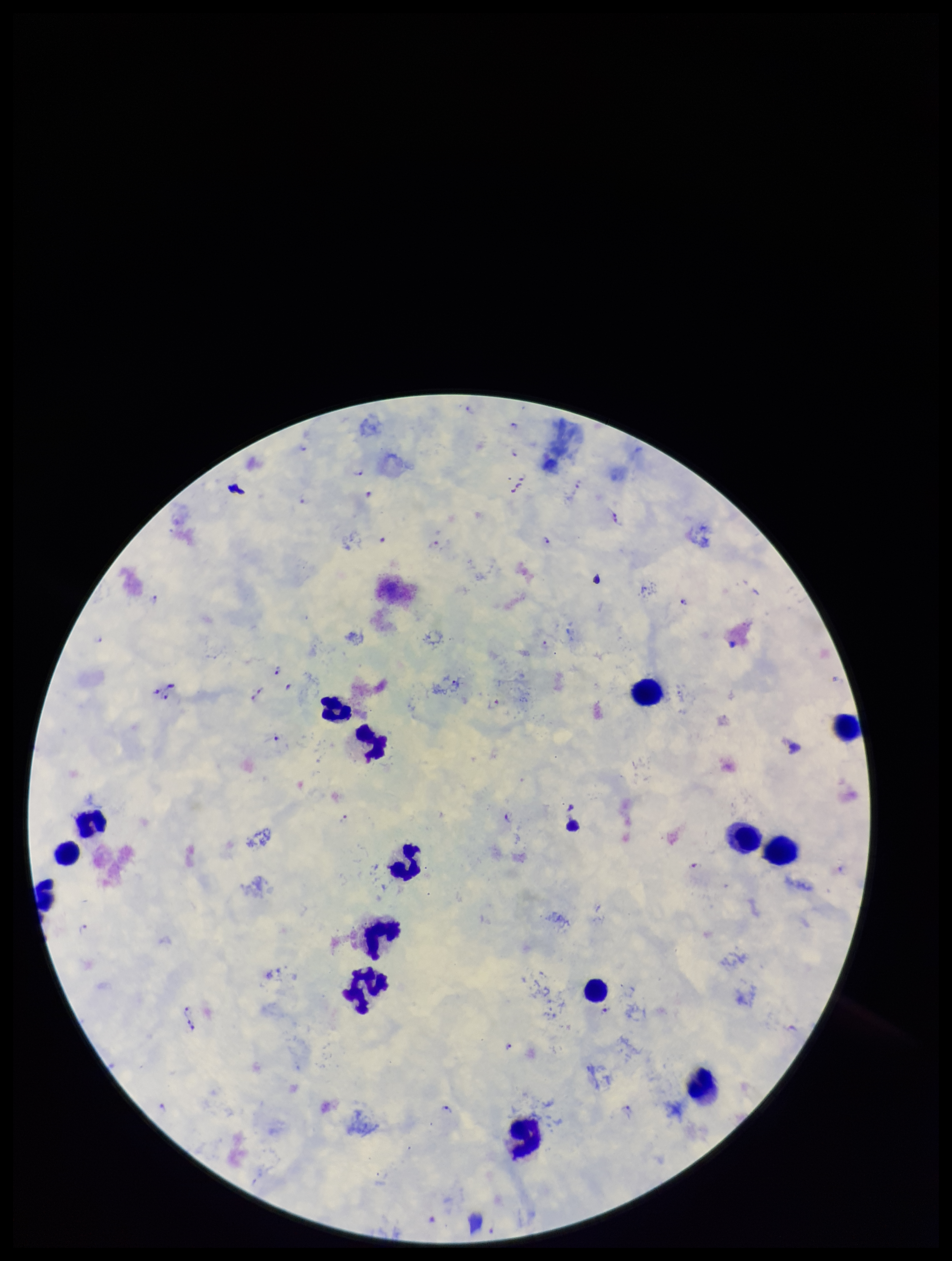
image_size: 952×1261 pixels
stain: Giemsa
capture: smartphone photograph through the microscope eyepiece
plasmodium_parasites: seen
preparation: thick smear
leukocyte_count: 15
field_of_view: single
parasite_count: 18
patient_malaria_status: positive
species_reported_for_this_patient: Plasmodium falciparum